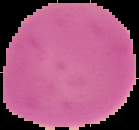

Result: negative for malaria parasites. Image is 139×130 pixels. The area outside the segmented cell region is set to black. From a thin blood smear.